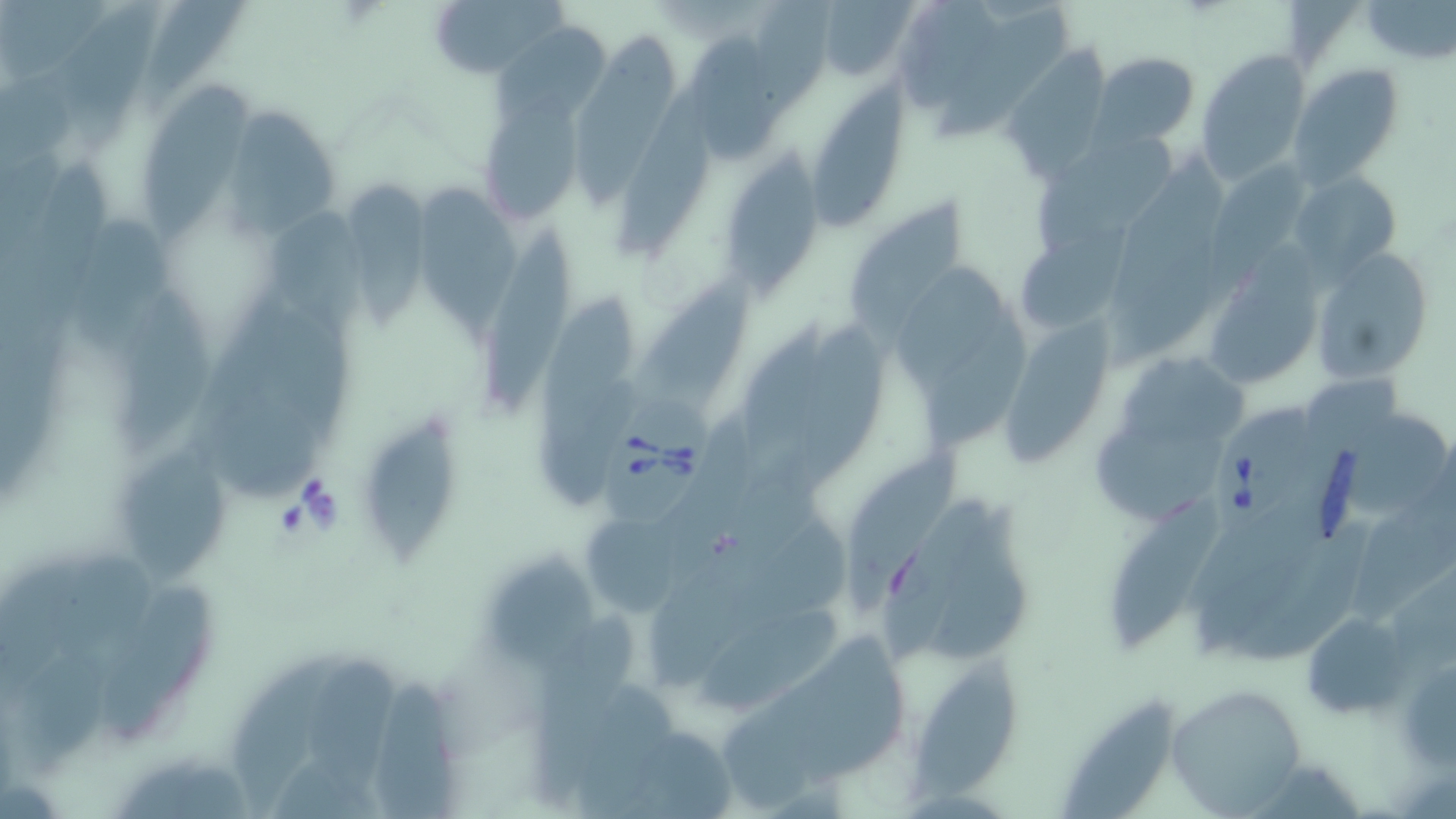
slide-level diagnosis = Babesia divergens
uninfected red blood cell locations = approximate bounding boxes as (x1, y1, x2, y2) in pixels: (141, 0, 255, 110), (429, 0, 563, 79), (59, 1, 172, 151), (748, 1, 838, 126), (813, 1, 917, 82), (902, 2, 1001, 106), (1359, 2, 1456, 64), (488, 20, 621, 129), (684, 27, 798, 164), (574, 33, 684, 209), (1002, 47, 1113, 179), (1196, 49, 1313, 185), (1092, 51, 1200, 148), (1289, 64, 1403, 185), (810, 80, 914, 233), (143, 84, 249, 251), (613, 84, 716, 267), (483, 92, 593, 224), (222, 107, 338, 237), (1035, 129, 1182, 247), (721, 158, 819, 293), (1211, 161, 1311, 267), (1291, 171, 1400, 272), (344, 179, 448, 334), (416, 184, 520, 343), (851, 196, 968, 339), (265, 214, 375, 340), (78, 221, 181, 362), (480, 221, 579, 413), (1020, 230, 1146, 330), (1312, 249, 1432, 386), (1205, 254, 1324, 392), (900, 261, 1014, 387), (630, 271, 765, 402), (532, 288, 643, 452), (103, 293, 216, 452), (924, 308, 1042, 457), (782, 320, 896, 493), (732, 322, 839, 461), (1008, 334, 1119, 462), (1117, 354, 1268, 448), (1300, 376, 1401, 455), (1091, 408, 1243, 528), (1339, 410, 1451, 521), (361, 413, 462, 572), (114, 441, 245, 586), (847, 449, 967, 617), (1347, 481, 1456, 626), (1105, 496, 1220, 643), (924, 505, 1036, 658), (583, 511, 684, 620), (491, 548, 597, 665), (86, 574, 212, 753), (685, 607, 851, 717), (1302, 610, 1413, 719), (519, 611, 643, 806), (233, 654, 335, 819), (905, 654, 1027, 804), (1397, 654, 1456, 771), (307, 659, 394, 798), (370, 676, 464, 819), (1166, 683, 1307, 816), (1059, 696, 1182, 819)
Babesia divergens-infected red blood cell locations = approximate bounding boxes as (x1, y1, x2, y2) in pixels: (603, 375, 719, 532), (1207, 399, 1323, 541)
magnification = 1000x
image size = 1456×819 pixels
field of view = one of a larger specimen
stain = May-Grünwald-Giemsa
modality = optical microscopy
preparation = thin blood film